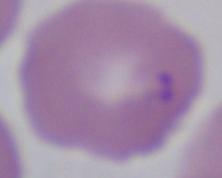
Summary:
  - Magnification: 1000x
  - Modality: photomicrograph
  - Identification: Babesia